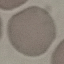
{
  "result": "no malaria parasites detected",
  "stain": "Giemsa",
  "capture": "smartphone through the microscope eyepiece",
  "preparation": "thin smear",
  "image_type": "cell patch, automatically extracted from a larger field of view and resized to 64 × 64 pixels"
}